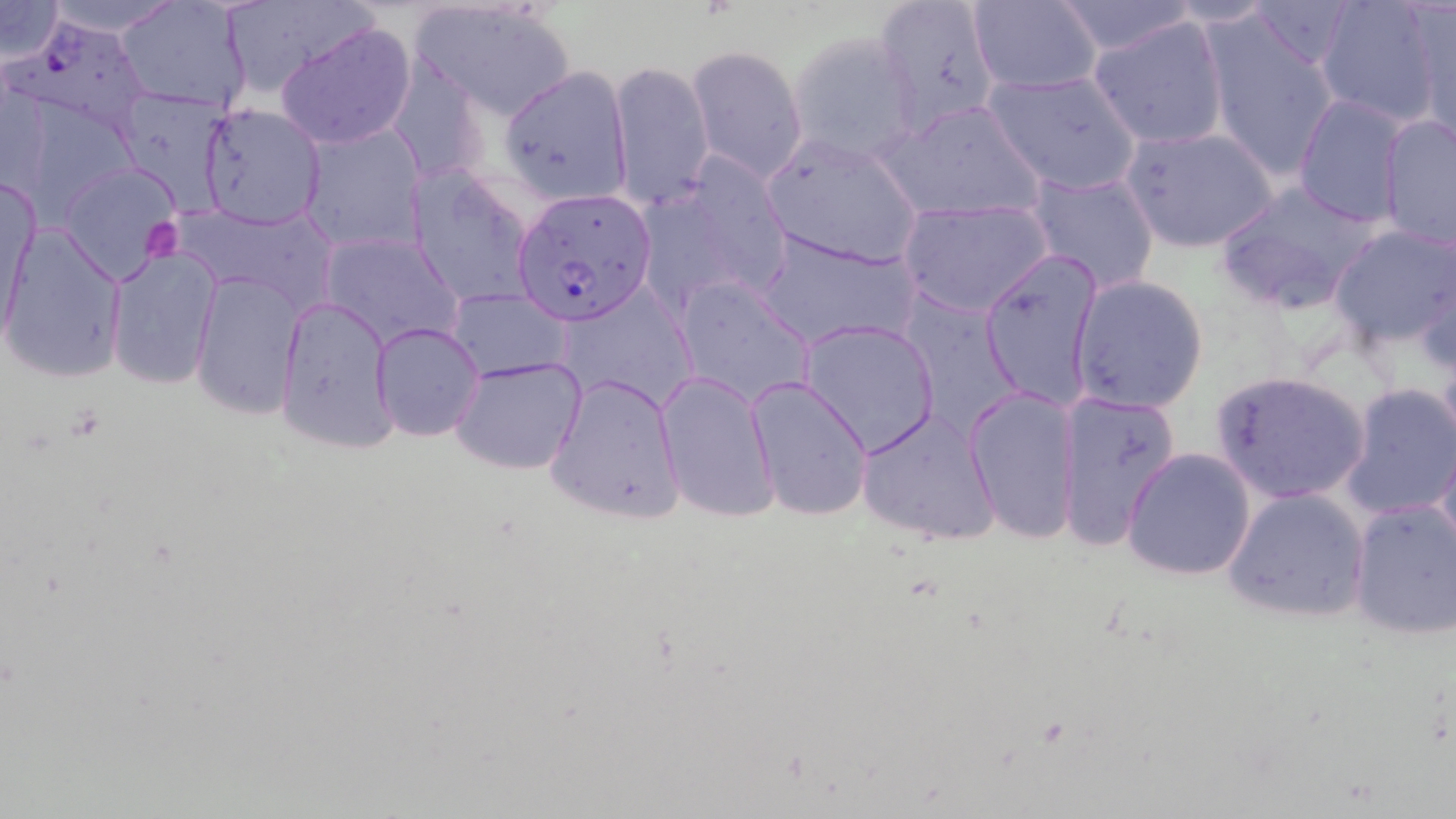

slide_level_diagnosis: Plasmodium falciparum
uninfected_red_blood_cell_locations: 'approximate bounding boxes as [x1, y1, x2, y2] in pixels: [32, 0, 190, 35], [115, 0, 254, 114], [871, 0, 1003, 136], [1242, 0, 1362, 70], [0, 1, 66, 62], [967, 1, 1102, 94], [1051, 1, 1200, 55], [1315, 1, 1445, 130], [1160, 2, 1281, 29], [1409, 3, 1455, 146], [410, 4, 576, 120], [1202, 15, 1342, 180], [1089, 16, 1230, 150], [276, 20, 417, 150], [787, 32, 920, 165], [688, 45, 810, 184], [609, 59, 714, 211], [391, 62, 489, 188], [500, 65, 634, 204], [983, 69, 1142, 196], [111, 89, 234, 215], [1292, 95, 1410, 226], [879, 98, 1046, 223], [199, 102, 328, 229], [1377, 114, 1456, 251], [298, 121, 426, 253], [1121, 124, 1277, 251], [761, 133, 923, 270], [654, 151, 793, 303], [59, 160, 185, 284], [409, 164, 537, 308], [1024, 169, 1161, 294], [1, 173, 36, 336], [1214, 181, 1383, 315], [898, 197, 1052, 319], [1328, 222, 1456, 348], [3, 227, 128, 384], [756, 229, 921, 350], [318, 233, 462, 351], [107, 246, 220, 390], [981, 248, 1104, 413], [1415, 251, 1454, 382], [189, 271, 304, 419], [1069, 274, 1209, 413], [672, 278, 813, 411], [449, 288, 570, 382], [276, 295, 396, 451], [800, 320, 941, 456], [372, 322, 484, 441], [450, 355, 587, 475], [1208, 369, 1372, 505], [655, 371, 781, 523], [545, 373, 686, 523], [745, 377, 873, 521], [1340, 382, 1456, 521], [965, 384, 1082, 545], [1053, 389, 1181, 551], [857, 408, 1000, 547], [1435, 431, 1456, 565], [1121, 447, 1255, 581], [1222, 487, 1371, 623], [1347, 498, 1456, 640]'
stain: May-Grünwald-Giemsa
preparation: thin blood film
plasmodium_falciparum_infected_red_blood_cell_locations: 'approximate bounding boxes as [x1, y1, x2, y2] in pixels: [9, 15, 158, 134], [511, 187, 656, 323]'
image_size: 1456×819 pixels
modality: light microscopy
magnification: 1000x
platelet_locations: 'approximate bounding boxes as [x1, y1, x2, y2] in pixels: [146, 220, 184, 260]'
field_of_view: one of a larger specimen